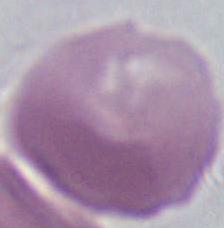
An erythrocyte is seen. Captured at 1000x magnification. Photomicrograph.